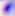
Summary:
  - Identification: Toxoplasma gondii
  - Magnification: 400x
  - Modality: photomicrograph